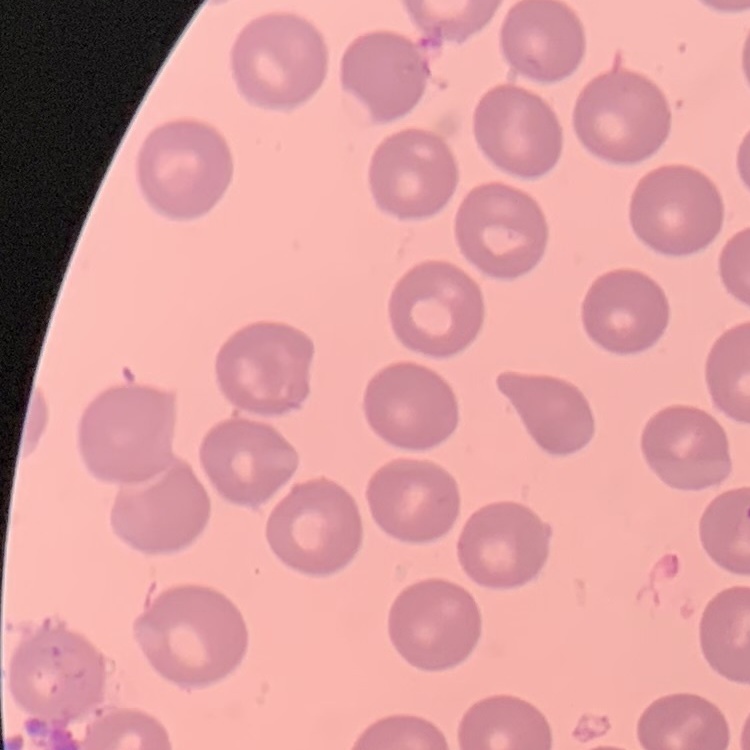
The erythrocytes exhibit no rouleaux formation. Thin peripheral smear. One tile cut from a larger photomicrograph. Stained with either Field's or Giemsa.